Identify the cell.
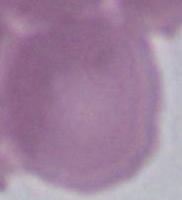

This is an erythrocyte.

modality: photomicrograph
magnification: 1000x